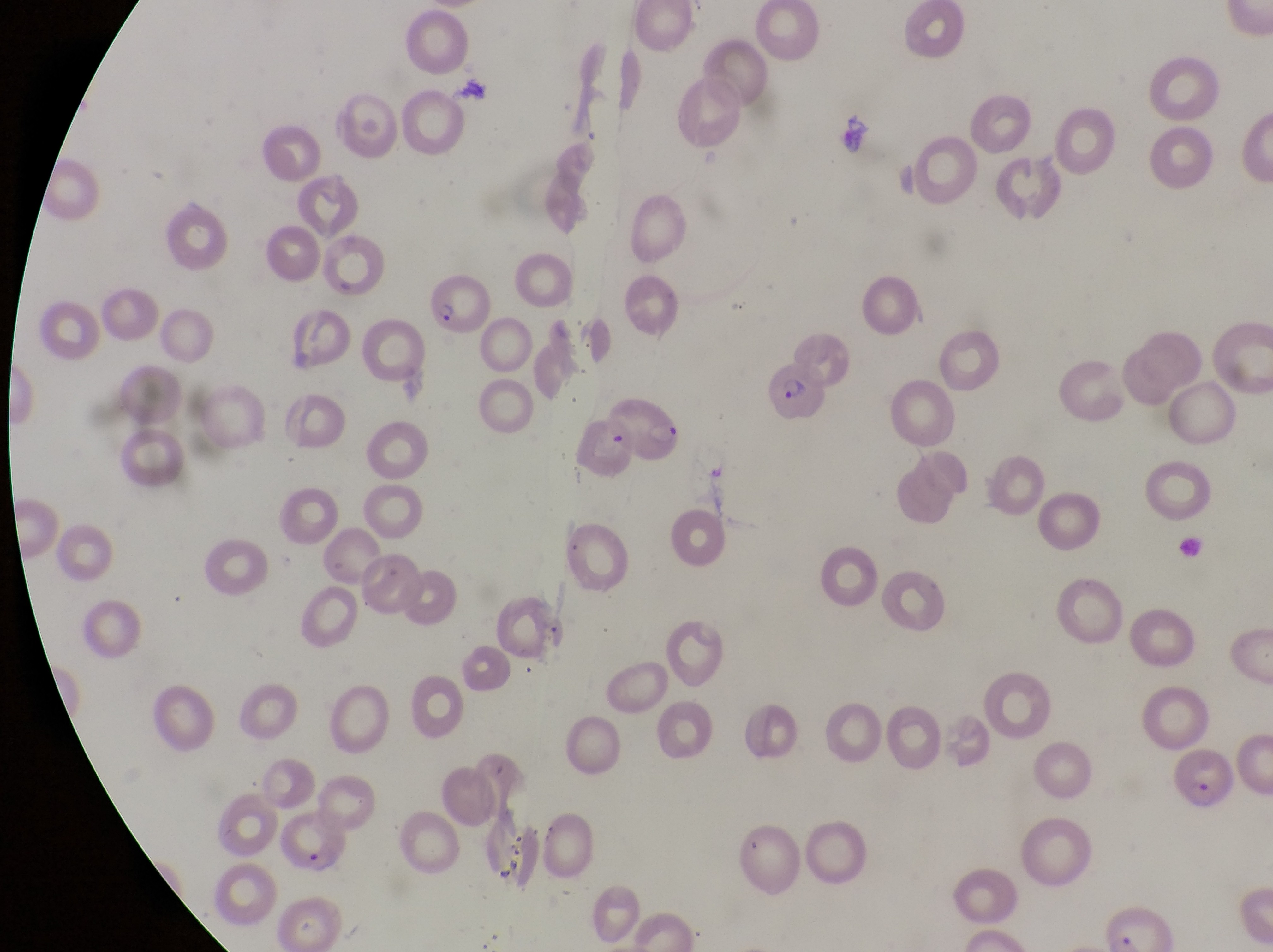
{
  "image_size": "1273×952 pixels",
  "magnification": "1000x",
  "country": "Uganda",
  "parasitised_red_blood_cell_locations": "approximate bounding boxes as {left, top, right, bottom} in pixels: {422, 277, 485, 340}, {764, 367, 833, 430}, {606, 387, 686, 469}, {1174, 749, 1237, 811}, {282, 815, 356, 877}",
  "field_of_view": "single",
  "capture": "smartphone photograph through the eyepiece of an Olympus CX-23 microscope",
  "preparation": "thin blood smear"
}